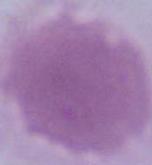
1000x magnification. A red blood cell is seen. Micrograph.